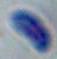
magnification = 1000x
modality = micrograph
identification = Toxoplasma gondii